Classify this cell by malaria status.
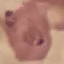
It is parasitized.

Summary:
  - Stain: Giemsa
  - Preparation: thin blood smear
  - Image type: cell patch, automatically extracted from a larger field of view and resized to 64 × 64 pixels
  - Capture: smartphone through the microscope eyepiece